Describe the morphology of the red blood cells.
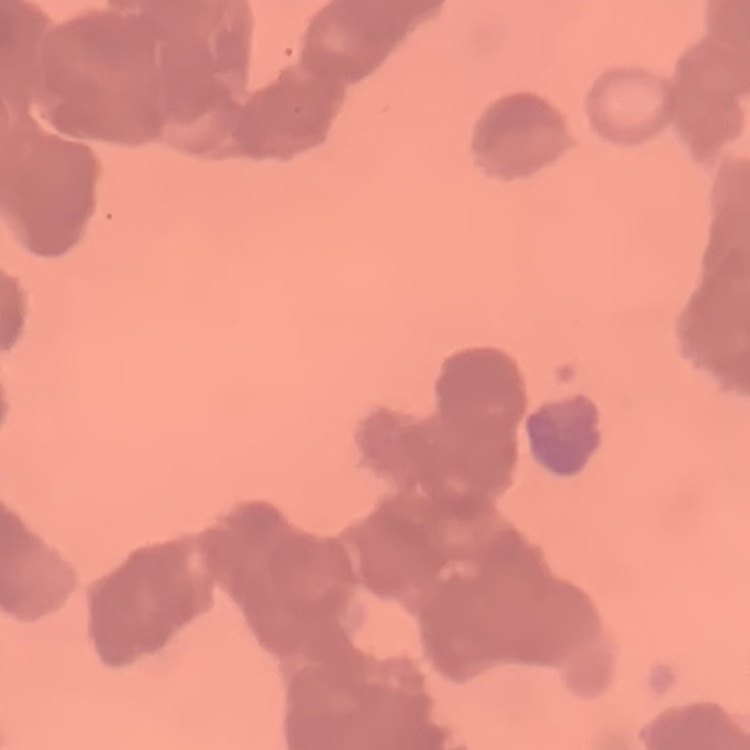
They show rouleaux formation.

Thin blood film. One tile cut from a larger photomicrograph. Stained with either Field's or Giemsa.